Classify this cell by malaria status.
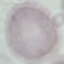
Uninfected.

Summary:
  - Image type: automatically extracted cell patch, resized to 64 × 64 pixels
  - Preparation: thin blood film
  - Stain: Giemsa
  - Capture: smartphone through the microscope eyepiece